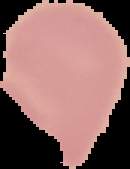

Summary:
  - Result: no malaria parasites detected
  - Image type: segmented cell region on a black background
  - Preparation: thin blood smear
  - Image size: 130×169 pixels